State the blood parasite species.
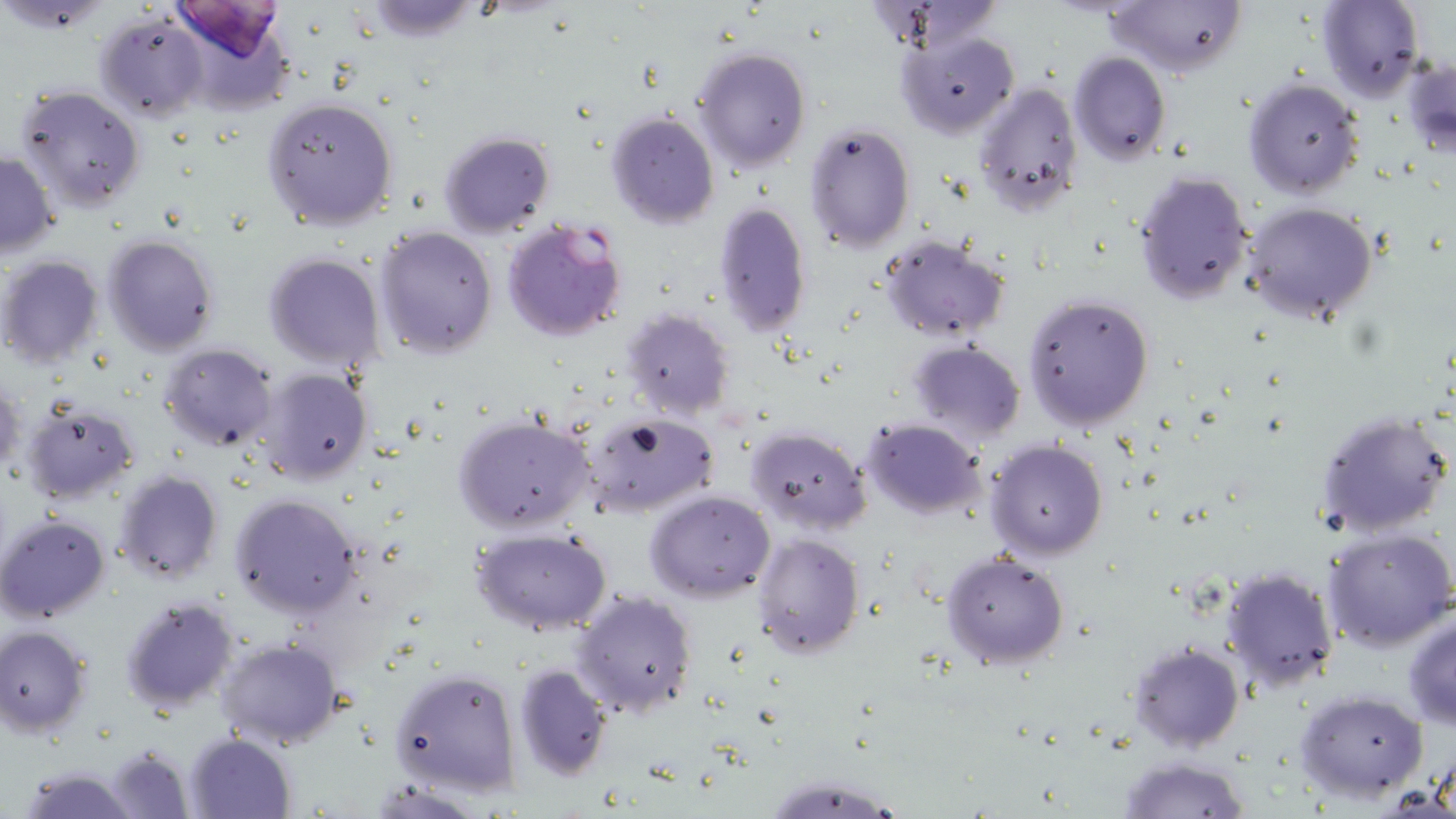
Plasmodium falciparum.

Summary:
  - Coordinate format: approximate bounding boxes as (x1,y1)-(x2,y2) corner pairs in pixels
  - Plasmodium falciparum-infected red blood cell locations: (501,217)-(626,343)
  - Uninfected red blood cell locations: (1104,0)-(1246,78), (1314,0)-(1426,101), (2,1)-(110,32), (353,1)-(487,41), (168,2)-(291,63), (94,9)-(210,121), (896,29)-(1019,138), (691,46)-(812,173), (1067,50)-(1172,165), (1402,55)-(1456,160), (1243,77)-(1366,200), (972,80)-(1084,215), (14,84)-(147,211), (261,95)-(400,231), (606,111)-(719,227), (804,122)-(917,254), (438,131)-(557,239), (1,150)-(60,258), (1133,171)-(1252,304), (1238,200)-(1378,326), (713,203)-(812,337), (374,225)-(498,359), (878,233)-(1011,343), (102,234)-(220,356), (263,252)-(384,372), (0,255)-(105,368), (1023,292)-(1156,432), (622,308)-(736,421), (906,339)-(1026,447), (160,344)-(278,452), (258,369)-(373,484), (0,378)-(25,484), (19,401)-(140,503), (579,410)-(719,519), (1314,411)-(1455,540), (454,414)-(597,535), (861,418)-(986,520), (746,425)-(872,532), (985,438)-(1109,559), (113,470)-(224,585), (646,490)-(776,603), (229,493)-(365,618), (0,511)-(111,623), (1323,526)-(1456,650), (470,527)-(613,635), (751,533)-(865,659), (941,551)-(1070,668), (1220,565)-(1341,694), (571,589)-(698,716), (120,596)-(238,714), (1403,610)-(1456,730), (1,625)-(91,735), (216,638)-(342,749), (1127,640)-(1246,753), (513,663)-(614,782), (391,665)-(523,797), (1295,688)-(1430,803), (184,732)-(294,817), (105,744)-(195,817), (1116,754)-(1251,819), (18,768)-(141,818)
  - Image size: 1456×819 pixels
  - Magnification: 1000x
  - Modality: optical microscopy
  - Preparation: thin blood smear
  - Field of view: one of a larger specimen
  - Stain: May-Grünwald-Giemsa